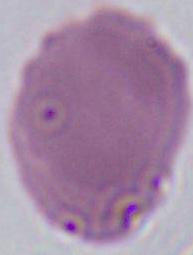
Summary:
  - Identification: red blood cell
  - Modality: photomicrograph
  - Magnification: 1000x